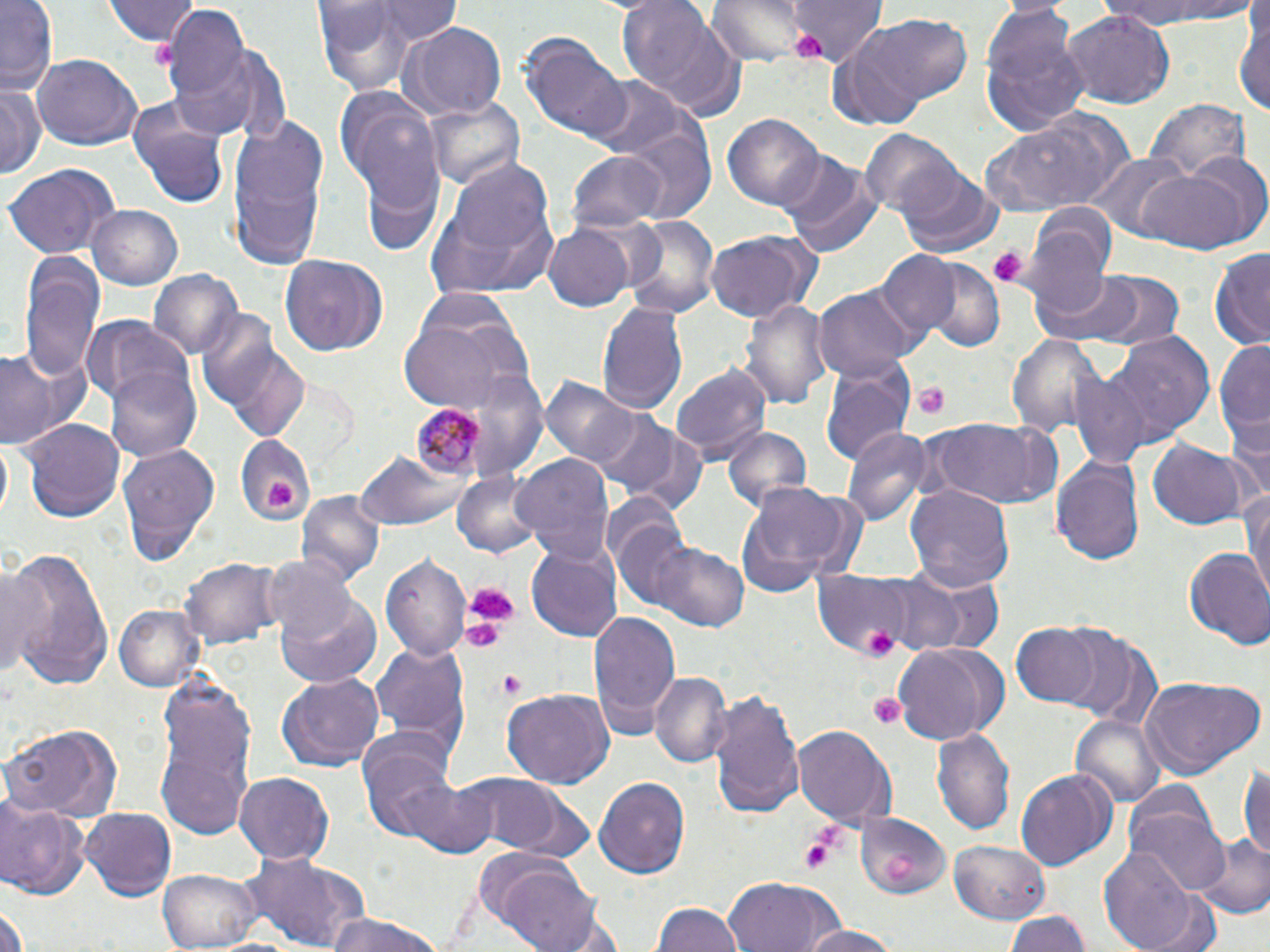

Summary:
  - Coordinate format: approximate bounding boxes as (x1,y1)-(x2,y2) corner pairs in pixels
  - Platelet locations: (796,33)-(825,63), (989,246)-(1026,287), (912,382)-(952,420), (265,479)-(293,509), (460,580)-(520,632), (460,616)-(509,654), (864,626)-(896,656), (498,669)-(527,699), (867,692)-(907,728), (801,835)-(836,875)
  - Plasmodium malariae-infected red blood cell locations: (405,400)-(498,482)
  - Uninfected red blood cell locations: (1,0)-(59,101), (106,0)-(198,46), (374,0)-(460,42), (615,0)-(740,115), (708,0)-(810,64), (789,0)-(886,67), (1103,0)-(1252,32), (157,3)-(261,135), (315,5)-(417,96), (979,6)-(1092,137), (1060,10)-(1177,108), (1234,12)-(1270,119), (847,15)-(978,112), (403,22)-(506,121), (519,32)-(634,145), (209,47)-(291,144), (32,55)-(141,152), (587,76)-(685,159), (333,82)-(446,214), (0,87)-(45,177), (421,96)-(526,190), (1146,97)-(1249,184), (129,98)-(229,208), (977,110)-(1130,215), (724,113)-(825,210), (228,117)-(329,267), (617,117)-(717,223), (861,130)-(959,216), (567,151)-(665,230), (775,151)-(883,257), (1180,152)-(1270,243), (355,153)-(446,260), (1090,155)-(1190,238), (431,157)-(563,296), (2,162)-(118,259), (1137,164)-(1253,255), (898,166)-(1004,257), (86,204)-(182,290), (1026,213)-(1116,317), (626,216)-(720,316), (544,225)-(634,310), (705,231)-(822,324), (1209,249)-(1270,350), (876,253)-(958,338), (18,255)-(103,385), (281,255)-(390,356), (920,260)-(1003,353), (149,269)-(243,362), (1090,271)-(1183,351), (1041,272)-(1145,345), (814,286)-(917,382), (741,294)-(833,409), (597,300)-(689,418), (397,306)-(531,412), (193,313)-(307,443), (83,320)-(192,408), (1114,333)-(1214,438), (1007,335)-(1106,437), (1213,336)-(1269,459), (0,342)-(91,453), (671,362)-(772,463), (465,367)-(548,479), (106,368)-(200,462), (822,373)-(911,468), (1071,373)-(1150,468), (544,376)-(641,472), (584,406)-(686,496), (1226,410)-(1270,501), (919,417)-(1063,511), (23,419)-(122,523), (613,421)-(709,510), (720,425)-(813,518), (843,426)-(933,524), (233,433)-(315,527), (1147,441)-(1255,531), (118,442)-(218,565), (356,450)-(470,533), (511,452)-(615,567), (1051,453)-(1146,567), (455,468)-(543,560), (740,481)-(869,591), (905,484)-(1013,593), (1241,485)-(1270,609), (297,490)-(385,584), (603,495)-(696,611), (526,540)-(623,644), (646,543)-(748,630), (1,548)-(115,690), (1182,548)-(1270,646), (382,552)-(472,665), (263,555)-(360,643), (181,558)-(282,649), (1,562)-(55,685), (871,567)-(1003,656), (813,569)-(925,656), (275,595)-(381,688), (112,604)-(206,692), (587,610)-(680,739), (1009,622)-(1105,707), (1047,626)-(1154,721), (367,639)-(471,752), (890,641)-(1008,744), (648,671)-(730,770), (275,673)-(382,771), (1137,675)-(1265,781), (153,685)-(256,840), (705,685)-(805,821), (502,689)-(612,789), (1070,714)-(1165,808), (2,721)-(123,821), (793,725)-(897,827), (933,726)-(1014,834), (360,740)-(466,846), (1238,763)-(1270,865), (1015,767)-(1116,871), (233,772)-(334,865), (451,773)-(582,857), (405,776)-(498,857), (595,777)-(690,878), (1,797)-(89,899), (78,806)-(176,899), (1128,807)-(1230,897), (853,809)-(954,900), (1193,833)-(1269,920), (951,840)-(1050,922), (1100,845)-(1203,952), (244,853)-(368,952), (496,864)-(606,952), (161,865)-(263,950), (723,878)-(841,952), (1,888)-(32,952), (1142,894)-(1222,952), (653,899)-(742,952), (1004,909)-(1091,952), (323,913)-(447,952), (793,923)-(905,952)
  - Slide-level diagnosis: Plasmodium malariae
  - Magnification: 1000x
  - Modality: light microscopy
  - Preparation: thin blood smear
  - Field of view: single
  - Stain: May-Grünwald-Giemsa
  - Image size: 1270×952 pixels